Name the parasite shown.
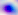
Toxoplasma gondii.

{
  "modality": "micrograph",
  "magnification": "400x"
}